Name the parasite shown.
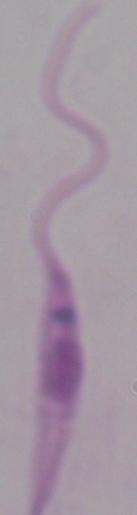

This is Leishmania.

Captured at 1000x magnification. Photomicrograph.